Assess this cell for malaria.
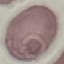

It is uninfected.

stain = Giemsa
capture = smartphone through the microscope eyepiece
preparation = thin blood film
image type = automatically extracted cell patch, resized to 64 × 64 pixels